Give the extent of all uninfected red blood cells.
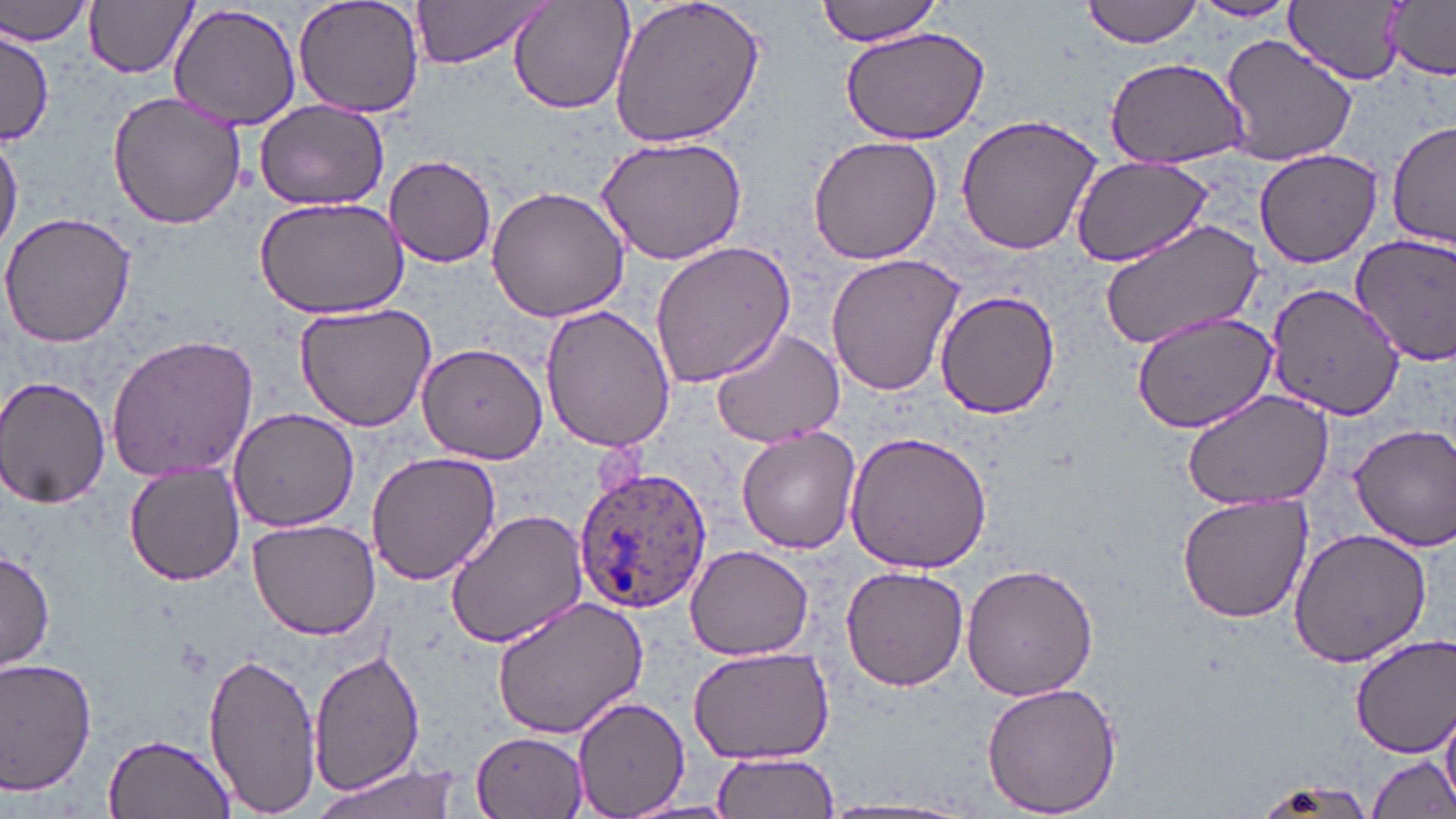

Approximate bounding boxes as [x1, y1, x2, y2] in pixels.
Uninfected red blood cells: [293, 0, 425, 119], [608, 0, 768, 151], [817, 0, 947, 46], [1082, 0, 1205, 47], [1190, 0, 1298, 24], [1286, 0, 1405, 84], [1379, 0, 1456, 81], [1, 1, 96, 47], [84, 1, 197, 79], [411, 1, 552, 67], [507, 1, 635, 115], [170, 5, 302, 130], [837, 22, 992, 146], [0, 30, 52, 144], [1218, 33, 1359, 165], [1104, 57, 1249, 167], [106, 91, 247, 230], [253, 101, 389, 212], [954, 111, 1104, 257], [1390, 120, 1456, 246], [0, 131, 22, 256], [594, 134, 748, 265], [808, 135, 942, 266], [1252, 145, 1387, 268], [385, 155, 497, 268], [1070, 156, 1213, 267], [485, 184, 629, 325], [253, 195, 410, 319], [0, 210, 136, 347], [1098, 220, 1266, 350], [1350, 231, 1456, 368], [648, 239, 796, 389], [825, 253, 966, 397], [1265, 282, 1404, 421], [933, 288, 1062, 421], [294, 300, 440, 432], [539, 303, 678, 454], [1128, 308, 1280, 434], [707, 325, 844, 448], [106, 334, 262, 480], [416, 342, 548, 463], [0, 375, 112, 510], [1181, 390, 1335, 512], [228, 408, 359, 533], [1350, 423, 1456, 551], [737, 427, 861, 553], [844, 434, 994, 575], [365, 451, 501, 585], [123, 464, 246, 586], [1175, 495, 1313, 623], [445, 508, 590, 649], [246, 518, 383, 640], [1288, 526, 1432, 669], [686, 543, 816, 659], [0, 547, 54, 673], [960, 561, 1100, 702], [841, 565, 968, 690], [490, 596, 649, 738], [1352, 634, 1456, 755], [687, 644, 835, 765], [202, 647, 323, 816], [309, 649, 424, 798], [0, 656, 98, 799], [979, 679, 1124, 817], [571, 698, 689, 819], [1440, 704, 1456, 809], [473, 730, 588, 817], [103, 732, 236, 819], [710, 752, 839, 818], [1365, 755, 1454, 819], [308, 760, 467, 819], [1250, 778, 1382, 819].

Summary:
  - Plasmodium ovale-infected red blood cell locations: [574, 463, 713, 612]
  - Slide-level diagnosis: Plasmodium ovale
  - Magnification: 1000x
  - Image size: 1456×819 pixels
  - Stain: May-Grünwald-Giemsa
  - Preparation: thin blood film
  - Modality: light microscopy
  - Field of view: single